State which parasite is depicted.
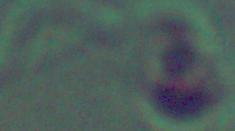
This is Leishmania.

Photomicrograph. 1000x magnification.